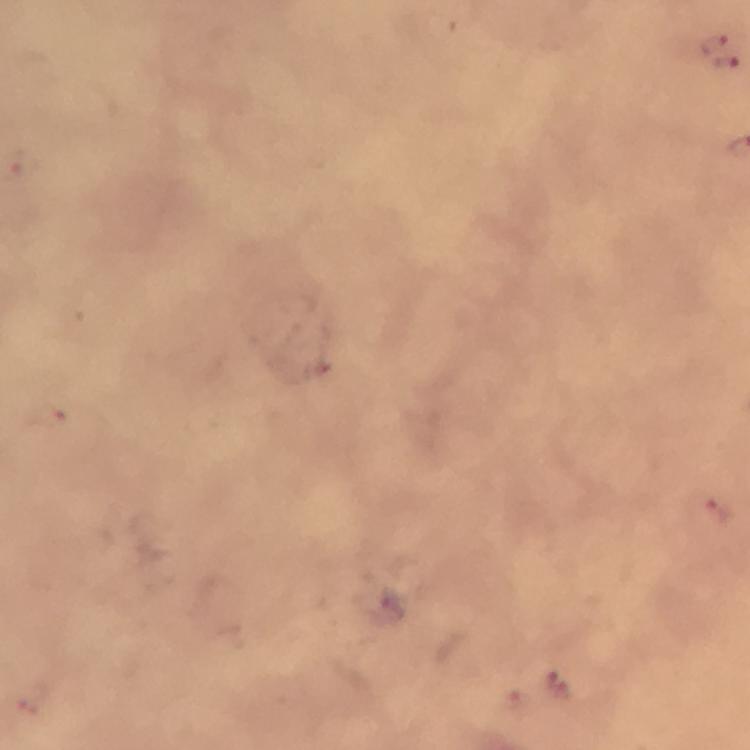

Approximate centers as {x, y} in pixels. Plasmodium parasite locations: {712, 43}, {726, 62}, {717, 508}, {557, 684}. Immersion oil was used. From a diagnostic examination for malaria. Cropped region of a single field of view. Giemsa stain. Smartphone photograph taken through a microscope. At 100x magnification. Image is 750×750 pixels. Thick blood film.